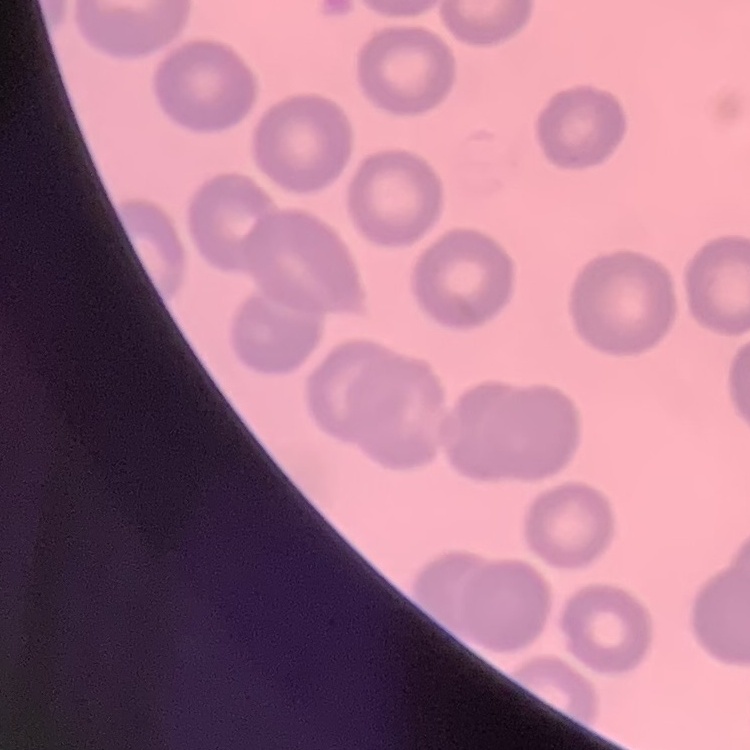

The red blood cells show no rouleaux formation. One tile cut from a larger photomicrograph. Thin blood smear. Stained with either Field's or Giemsa.